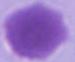

Summary:
  - Modality: micrograph
  - Identification: red blood cell
  - Magnification: 1000x